Report the malaria status of this cell.
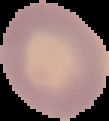

Uninfected.

From a thin blood smear. Segmented cell region on a black background. Image is 109×121 pixels.